Point out each Plasmodium parasite.
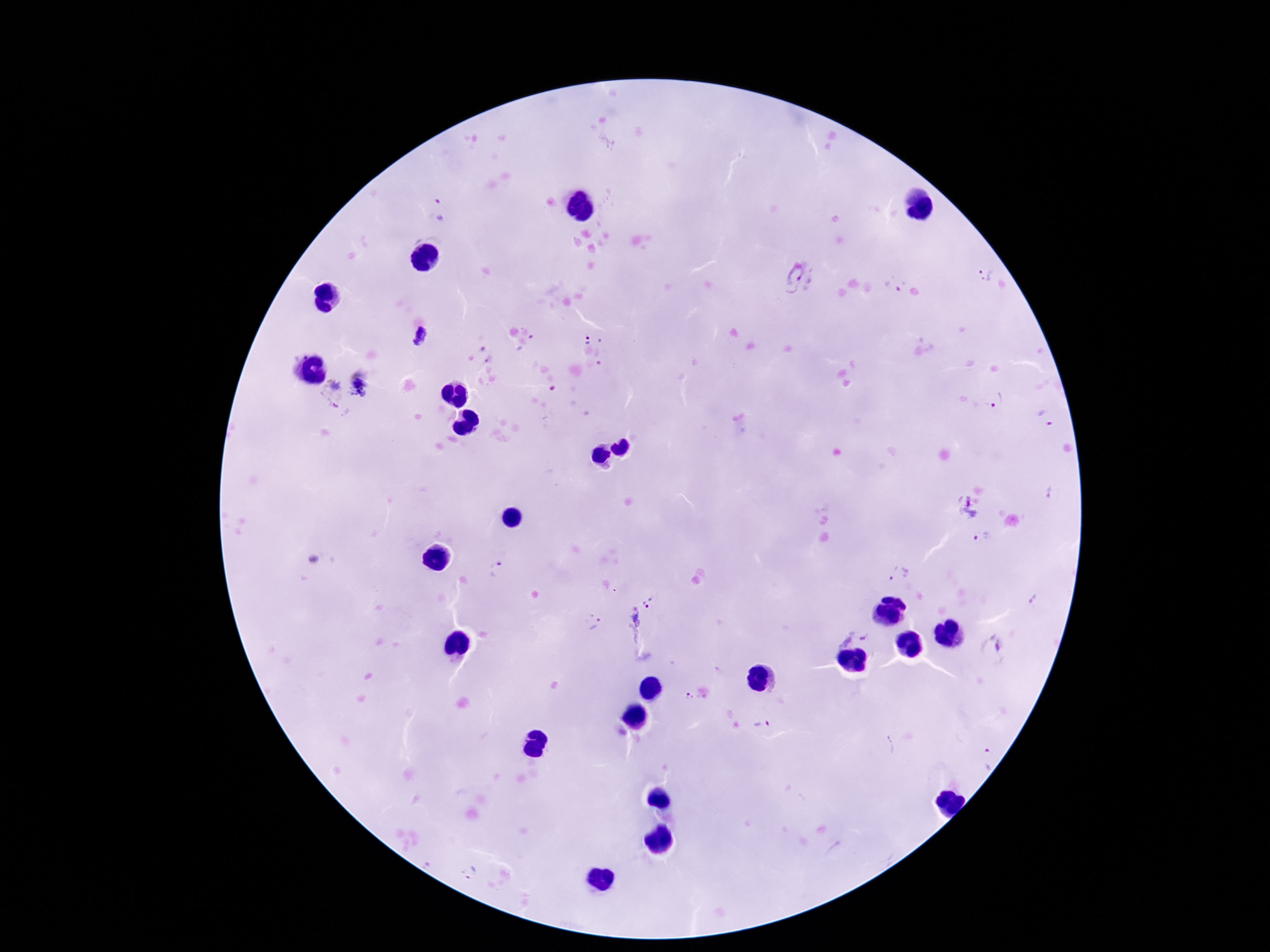
Approximate centers as {x, y} in pixels.
Plasmodium parasites: {441, 209}, {987, 274}, {800, 278}, {422, 336}, {588, 338}, {360, 388}, {334, 393}, {996, 400}, {1044, 417}, {968, 507}, {983, 537}, {900, 574}, {650, 601}, {593, 622}, {636, 628}, {855, 634}, {992, 647}, {691, 697}, {764, 725}, {469, 873}.

Summary:
  - Capture: smartphone camera through the microscope eyepiece
  - Preparation: thick blood film
  - Image size: 1270×952 pixels
  - Patient malaria status: infected
  - Stain: Giemsa
  - Magnification: 100x
  - Field of view: single